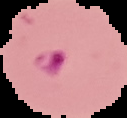

image type = segmented cell region with the area outside set to black
malaria status = parasitized
preparation = thin blood film
image size = 127×118 pixels